Outline each blood parasite and name the species.
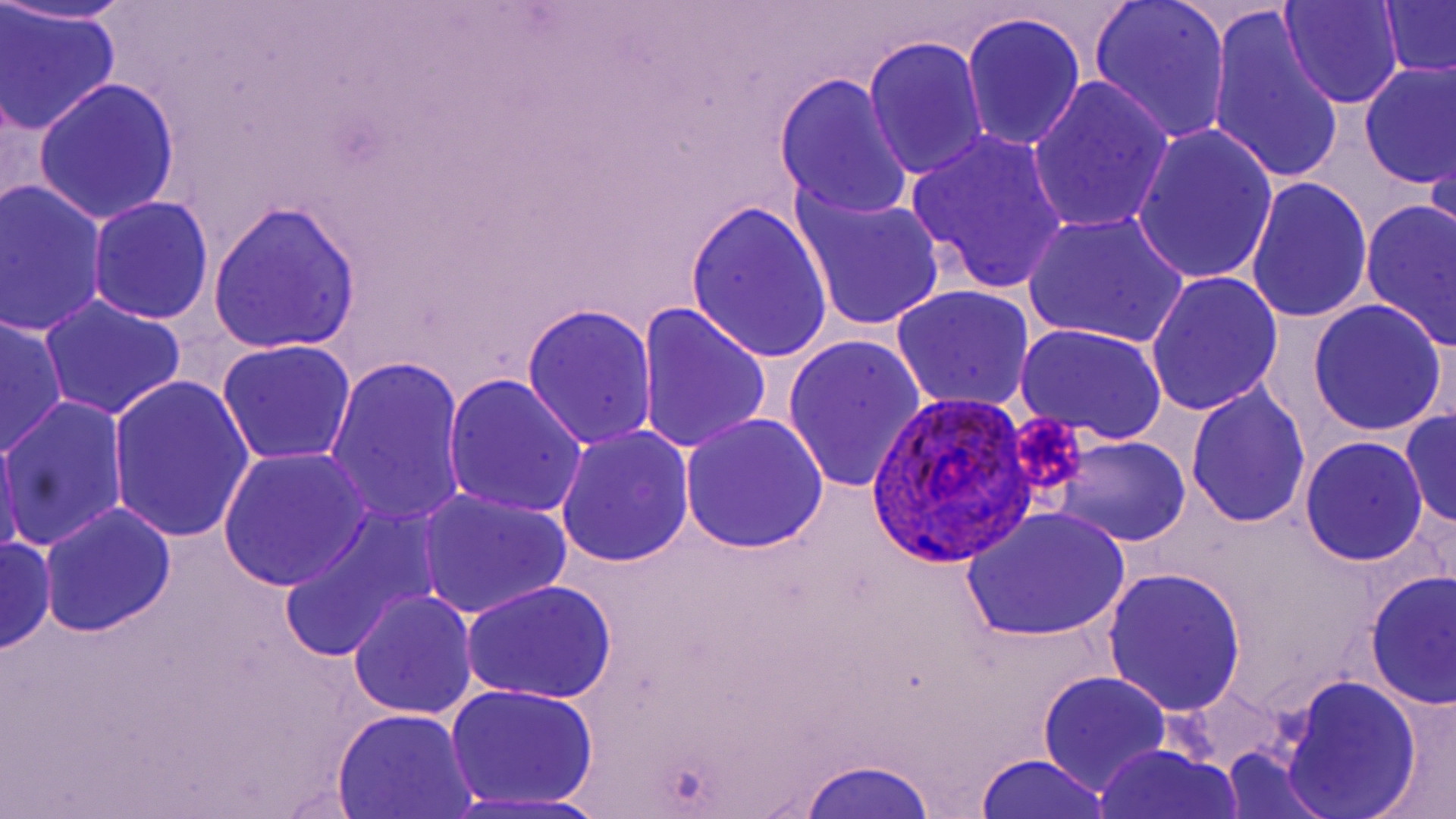
Approximate bounding boxes as (x1, y1, x2, y2) in pixels.
Plasmodium ovale-infected red blood cells: (869, 388, 1036, 570).
No Plasmodium falciparum, Plasmodium malariae, Plasmodium vivax, Babesia divergens, or Trypanosoma brucei observed.

slide_level_diagnosis: Plasmodium ovale
magnification: 1000x
platelet_locations: 'approximate bounding boxes as (x1, y1, x2, y2) in pixels: (1005, 409, 1090, 499)'
field_of_view: one of a larger specimen
modality: optical microscopy
uninfected_red_blood_cell_locations: 'approximate bounding boxes as (x1, y1, x2, y2) in pixels: (1, 0, 143, 25), (1087, 0, 1232, 144), (1279, 0, 1404, 109), (1377, 1, 1456, 83), (1, 6, 121, 135), (1208, 9, 1346, 188), (961, 13, 1086, 154), (864, 36, 988, 182), (1357, 59, 1455, 190), (773, 73, 914, 221), (32, 78, 181, 225), (1027, 78, 1176, 235), (1132, 125, 1280, 287), (905, 129, 1070, 295), (1427, 131, 1456, 268), (1246, 177, 1373, 325), (1, 181, 109, 336), (789, 184, 949, 336), (86, 196, 214, 326), (686, 198, 834, 367), (1360, 198, 1456, 352), (209, 200, 363, 354), (1023, 213, 1190, 348), (1145, 271, 1284, 415), (890, 285, 1035, 412), (39, 294, 187, 421), (1306, 298, 1448, 438), (637, 303, 772, 457), (522, 304, 657, 450), (0, 314, 68, 459), (1015, 322, 1168, 444), (782, 332, 927, 496), (216, 340, 356, 466), (325, 356, 468, 530), (108, 375, 257, 546), (443, 375, 589, 519), (1185, 383, 1310, 528), (1, 394, 128, 554), (1399, 409, 1456, 534), (678, 414, 828, 556), (0, 424, 22, 564), (556, 425, 694, 566), (1049, 437, 1192, 547), (1300, 437, 1428, 565), (219, 451, 370, 589), (416, 489, 572, 620), (39, 502, 177, 637), (281, 508, 436, 663), (961, 508, 1132, 643), (1, 533, 54, 656), (1102, 566, 1247, 717), (1365, 570, 1455, 711), (461, 578, 619, 705), (348, 591, 478, 720), (1037, 672, 1172, 796), (1276, 673, 1424, 818), (445, 684, 601, 809), (1369, 694, 1456, 819), (332, 709, 482, 819), (1093, 744, 1244, 819), (1220, 748, 1334, 818), (973, 752, 1117, 818), (796, 756, 939, 818), (447, 790, 615, 819)'
preparation: thin blood film
stain: May-Grünwald-Giemsa
image_size: 1456×819 pixels